Identify the cell.
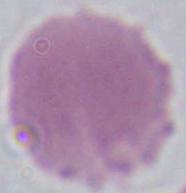
This is an erythrocyte.

Photomicrograph. 1000x magnification.